Outline each Plasmodium vivax-infected red blood cell.
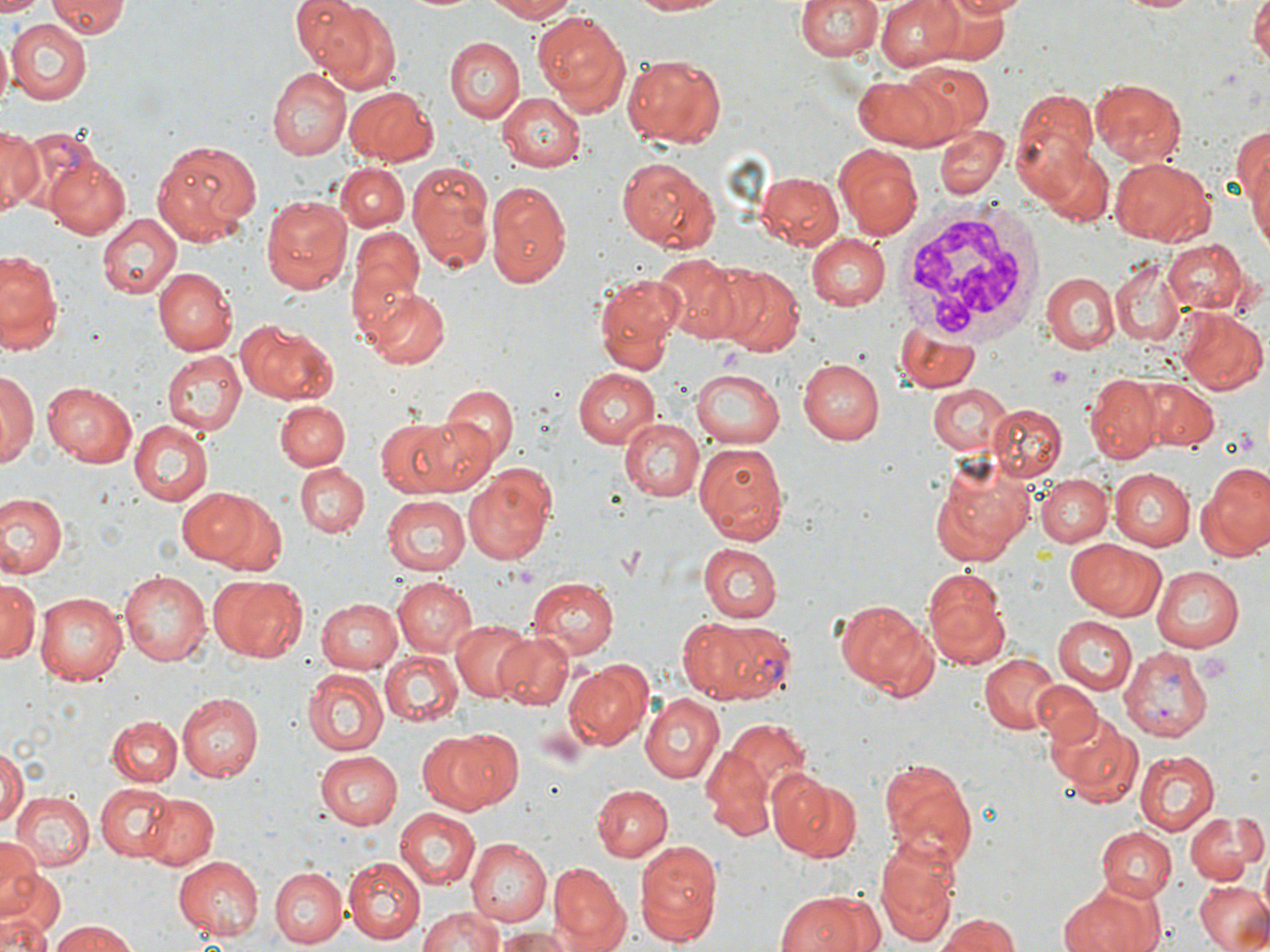
Approximate bounding boxes as (x1,y1)-(x2,y2) corner pairs in pixels.
Plasmodium vivax-infected red blood cells: (10,126)-(102,215), (676,615)-(798,704), (1120,649)-(1213,741).

{
  "slide_level_diagnosis": "Plasmodium vivax",
  "platelet_locations": "approximate bounding boxes as (x1,y1)-(x2,y2) corner pairs in pixels: (1197,653)-(1234,683)",
  "white_blood_cell_locations": "approximate bounding boxes as (x1,y1)-(x2,y2) corner pairs in pixels: (897,202)-(1050,346)",
  "preparation": "thin blood film",
  "uninfected_red_blood_cell_locations": "approximate bounding boxes as (x1,y1)-(x2,y2) corner pairs in pixels: (0,0)-(46,16), (47,0)-(128,40), (294,0)-(388,83), (484,0)-(583,22), (626,0)-(731,16), (797,0)-(882,63), (875,0)-(968,70), (915,0)-(1014,66), (1250,0)-(1270,73), (531,10)-(630,117), (6,21)-(89,104), (444,39)-(523,121), (622,54)-(728,149), (898,60)-(994,140), (267,68)-(350,160), (850,75)-(961,149), (1089,78)-(1187,167), (344,85)-(438,167), (1011,88)-(1099,196), (499,89)-(586,172), (935,125)-(1009,200), (0,127)-(43,212), (1242,134)-(1270,263), (151,138)-(262,243), (832,144)-(923,238), (1029,146)-(1116,227), (616,155)-(721,253), (47,156)-(130,238), (1110,158)-(1214,247), (407,159)-(497,269), (337,164)-(411,231), (757,172)-(846,251), (488,178)-(573,291), (260,193)-(353,296), (97,213)-(182,299), (346,228)-(425,321), (805,232)-(890,310), (1163,238)-(1249,316), (0,247)-(64,356), (657,254)-(748,343), (1110,257)-(1184,348), (710,265)-(803,355), (154,267)-(236,355), (1041,272)-(1117,354), (595,273)-(685,371), (363,288)-(450,368), (1177,310)-(1266,394), (237,322)-(340,405), (898,328)-(982,389), (161,350)-(245,435), (801,357)-(885,445), (690,367)-(784,446), (572,368)-(661,449), (1,369)-(38,467), (1085,375)-(1161,461), (43,380)-(138,467), (1138,380)-(1220,452), (442,383)-(519,465), (928,383)-(1012,457), (281,399)-(361,535), (276,400)-(349,471), (986,404)-(1066,480), (401,413)-(495,494), (375,418)-(458,497), (618,418)-(704,502), (129,422)-(210,505), (691,441)-(788,548), (1195,461)-(1270,561), (292,463)-(366,538), (462,465)-(557,564), (928,465)-(1035,566), (1110,467)-(1195,550), (1036,473)-(1111,546), (180,486)-(276,571), (0,494)-(65,578), (381,494)-(469,575), (1067,538)-(1167,622), (697,542)-(782,623), (1142,562)-(1232,730), (1151,565)-(1243,652), (920,567)-(1010,662), (119,569)-(210,664), (209,576)-(304,661), (393,576)-(477,657), (528,576)-(620,659), (1,577)-(40,659), (36,592)-(128,686), (832,596)-(937,700), (315,597)-(404,674), (1054,615)-(1137,695), (450,619)-(536,700), (492,632)-(574,712), (379,652)-(462,725), (979,653)-(1062,735), (564,661)-(653,750), (302,670)-(388,754), (1031,681)-(1103,747), (175,690)-(261,783), (641,692)-(726,783), (1051,715)-(1142,807), (108,716)-(183,786), (721,717)-(816,818), (421,729)-(517,813), (0,748)-(24,833), (314,750)-(403,830), (1135,750)-(1220,835), (702,752)-(773,839), (879,754)-(978,864), (767,769)-(862,863), (93,783)-(175,860), (591,784)-(673,862), (12,791)-(94,870), (141,793)-(220,870), (392,808)-(480,889), (1182,811)-(1263,883), (1095,826)-(1176,904), (0,837)-(45,916), (469,837)-(553,926), (635,840)-(723,947), (874,841)-(959,949), (173,856)-(266,937), (343,856)-(425,941), (548,863)-(628,950), (269,867)-(347,947), (1,869)-(65,948), (1194,880)-(1270,952), (1057,881)-(1167,952), (776,889)-(887,952), (418,907)-(506,952), (0,908)-(57,952), (934,911)-(1025,952), (45,919)-(141,952), (493,928)-(577,952)",
  "stain": "May-Grünwald-Giemsa",
  "modality": "light microscopy",
  "field_of_view": "one of a larger specimen",
  "magnification": "1000x",
  "image_size": "1270×952 pixels"
}